Identify the parasite.
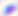

Toxoplasma gondii.

magnification = 400x
modality = photomicrograph